Classify this cell by malaria status.
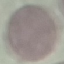
It is uninfected.

Photographed with a smartphone camera at the microscope eyepiece. Cell patch, automatically extracted from a larger field of view and resized to 64 × 64 pixels. Thin blood smear. Giemsa stain.